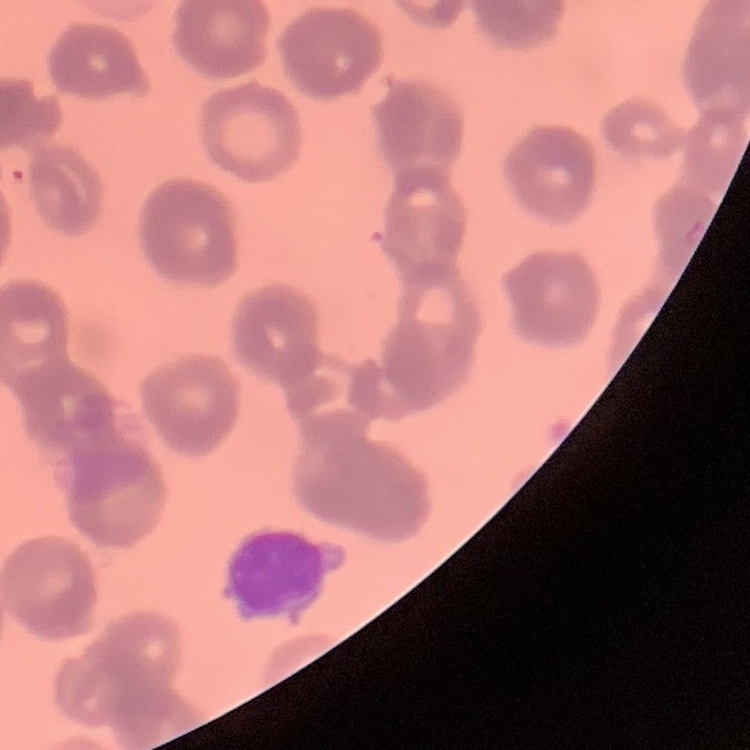

The erythrocytes show rouleaux formation. Field's or Giemsa stain. One tile cut from a larger photomicrograph. Thin blood smear.